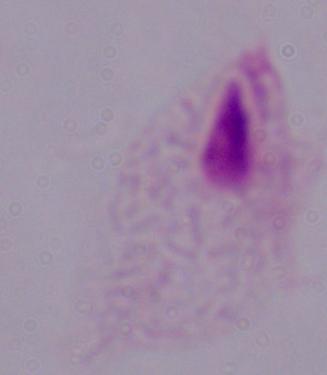

1000x magnification. A trichomonad is seen. Photomicrograph.